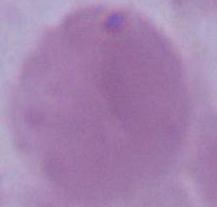
magnification = 1000x
identification = erythrocyte
modality = micrograph